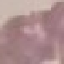

{
  "malaria_status": "uninfected",
  "preparation": "thin smear",
  "stain": "Giemsa",
  "image_type": "cell patch, automatically extracted from a larger field of view and resized to 64 × 64 pixels",
  "capture": "smartphone camera at the microscope eyepiece"
}